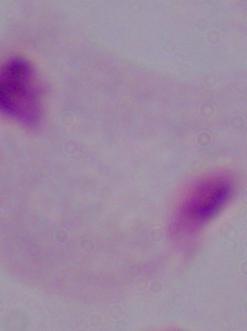
Summary:
  - Magnification: 1000x
  - Modality: micrograph
  - Identification: trichomonad